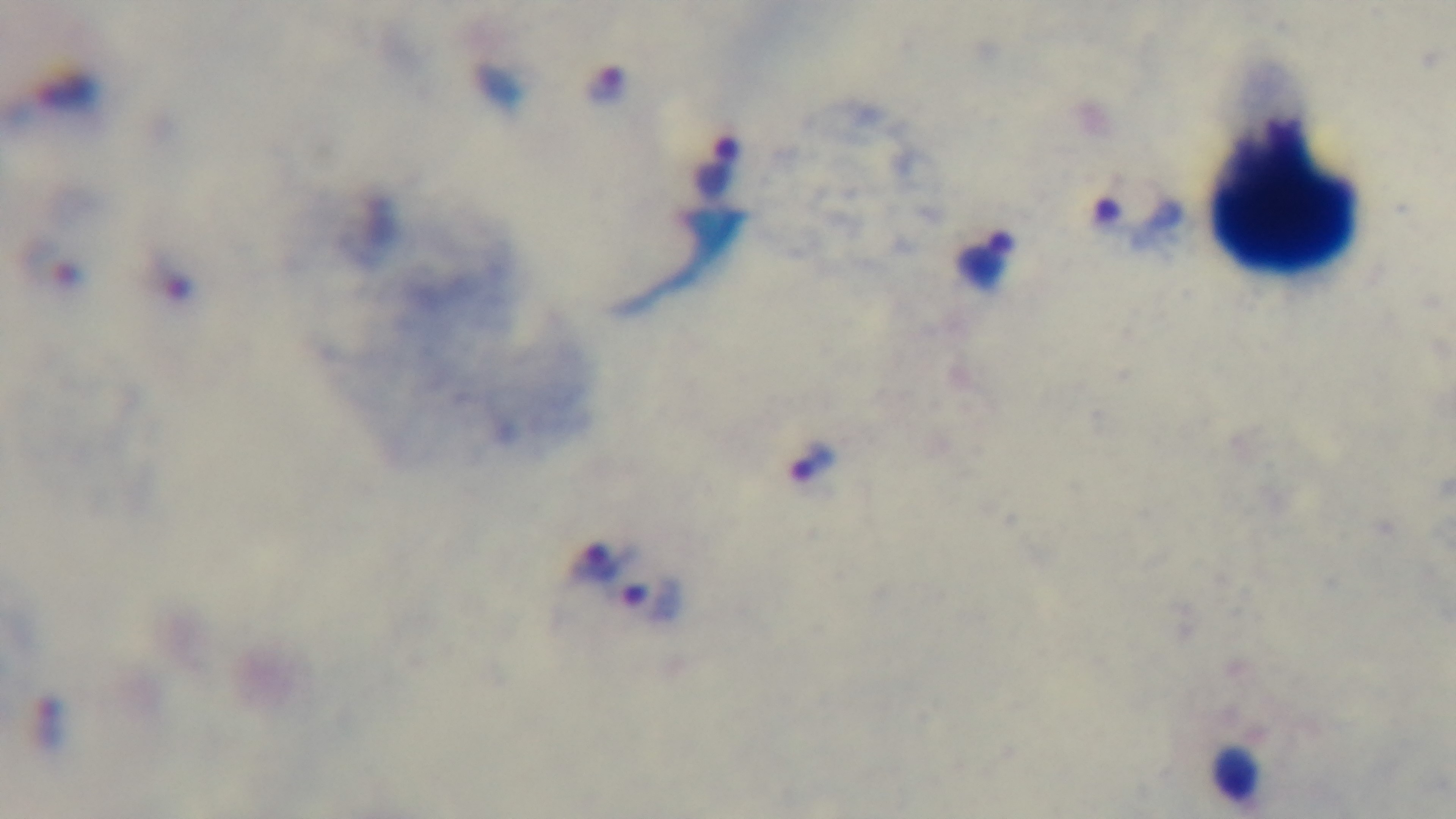
Malaria status: infected. Giemsa stain. 100x oil-immersion objective. Light microscopy. Single field of view. Captured with a mounted 4K digital camera. Preparation: thick smear.